Name the parasite shown.
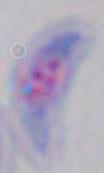

Toxoplasma gondii.

Captured at 1000x magnification. Photomicrograph.